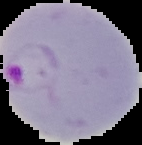
image size = 142×145 pixels
malaria status = parasitized
preparation = thin blood film
image type = segmented cell region with the area outside set to black